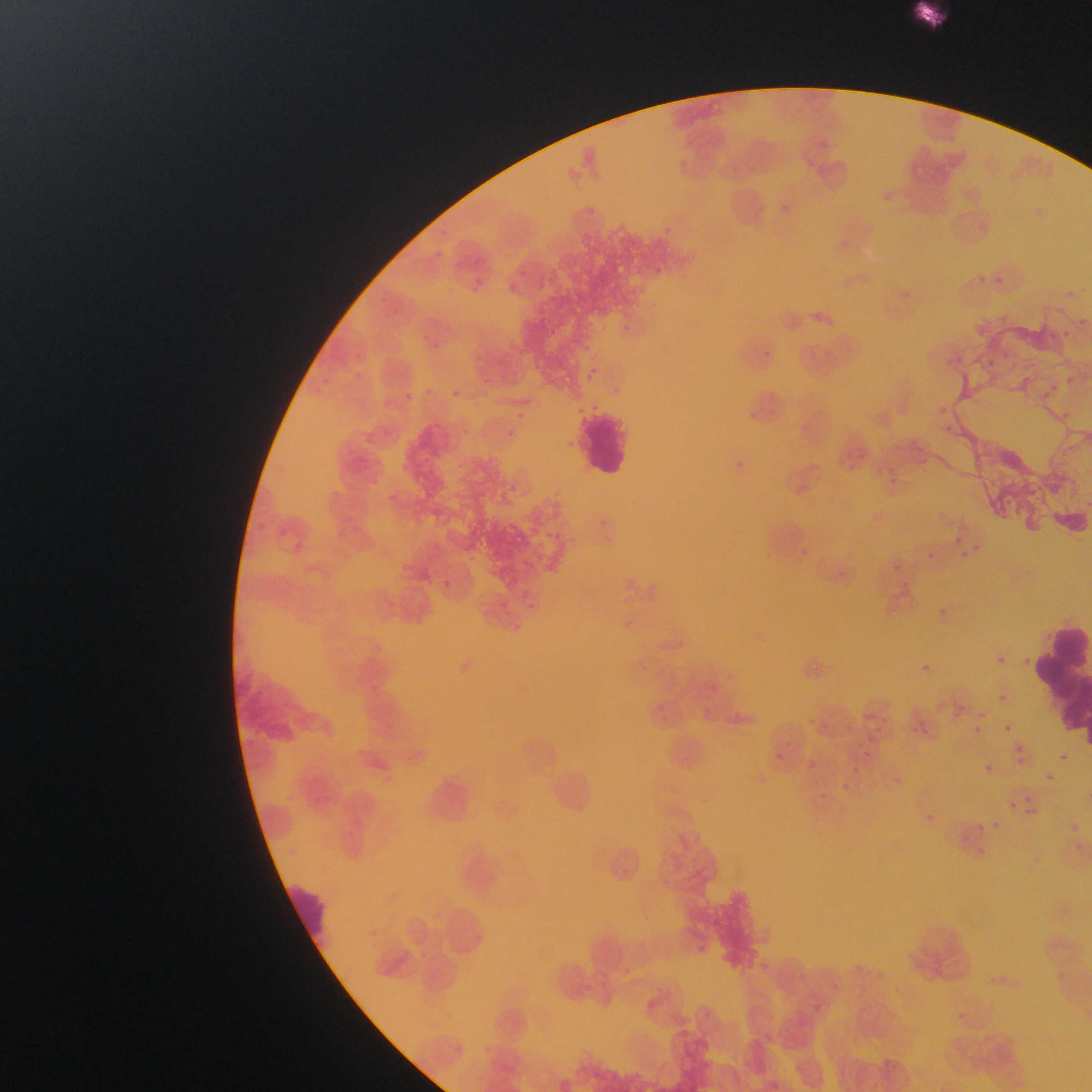

Approximate bounding boxes as {left, top, right, bottom} in pixels.
Summary:
  - Malaria parasite locations: {666, 223, 671, 232}, {432, 250, 447, 263}, {655, 266, 664, 275}, {517, 271, 524, 281}, {997, 272, 1009, 286}, {476, 276, 490, 291}, {510, 280, 515, 294}, {621, 321, 635, 337}, {546, 325, 562, 340}, {423, 329, 443, 347}, {1059, 329, 1073, 340}, {764, 347, 774, 361}, {1001, 347, 1011, 359}, {987, 358, 995, 374}, {589, 363, 607, 374}, {580, 370, 600, 385}, {354, 371, 367, 386}, {1066, 375, 1078, 388}, {483, 377, 491, 384}, {1051, 379, 1062, 388}, {612, 386, 623, 396}, {452, 387, 462, 397}, {1045, 388, 1056, 399}, {400, 390, 418, 404}, {1060, 408, 1074, 423}, {512, 409, 527, 423}, {750, 411, 759, 417}, {942, 421, 961, 436}, {505, 429, 523, 437}, {568, 438, 579, 452}, {735, 457, 744, 472}, {397, 463, 412, 473}, {370, 474, 382, 484}, {889, 477, 904, 486}, {509, 482, 520, 493}, {1006, 493, 1012, 505}, {1005, 506, 1028, 518}, {599, 514, 610, 525}, {545, 531, 555, 539}, {956, 535, 965, 543}, {974, 541, 989, 552}, {798, 545, 810, 558}, {959, 550, 970, 558}, {927, 552, 937, 566}, {468, 554, 479, 565}, {893, 562, 905, 572}, {834, 566, 849, 577}, {443, 578, 456, 590}, {906, 582, 916, 588}, {526, 601, 533, 611}, {930, 603, 951, 623}, {626, 617, 636, 633}, {514, 620, 523, 629}, {999, 652, 1009, 665}, {914, 659, 935, 678}, {998, 695, 1006, 703}, {957, 700, 969, 709}, {978, 708, 991, 722}, {866, 709, 879, 719}, {883, 715, 892, 726}, {969, 722, 984, 738}, {1002, 722, 1015, 734}, {910, 723, 915, 733}, {919, 726, 931, 735}, {863, 735, 873, 744}, {1019, 743, 1028, 754}, {1055, 750, 1071, 765}, {859, 751, 875, 758}, {775, 752, 784, 759}, {1015, 758, 1026, 767}, {806, 759, 817, 769}, {981, 762, 995, 776}, {849, 764, 859, 772}, {1041, 770, 1056, 785}, {892, 773, 910, 792}, {841, 778, 850, 792}, {819, 786, 833, 800}, {1006, 797, 1024, 813}, {1025, 806, 1040, 816}, {924, 809, 938, 822}, {992, 817, 998, 835}, {976, 821, 986, 832}, {1070, 821, 1083, 834}, {957, 831, 971, 845} | approximate {x, y} pixel centers of objects too small to bound: {1083, 321}, {922, 719}
  - Leukocyte locations: {909, 2, 950, 33}, {578, 410, 634, 477}, {1049, 620, 1088, 664}, {1027, 655, 1090, 699}, {1056, 690, 1092, 728}, {283, 877, 333, 955}
  - Field of view: single
  - Capture: mobile-phone photograph through a microscope
  - Image size: 1092×1092 pixels
  - Country: Ghana
  - Preparation: thin blood smear